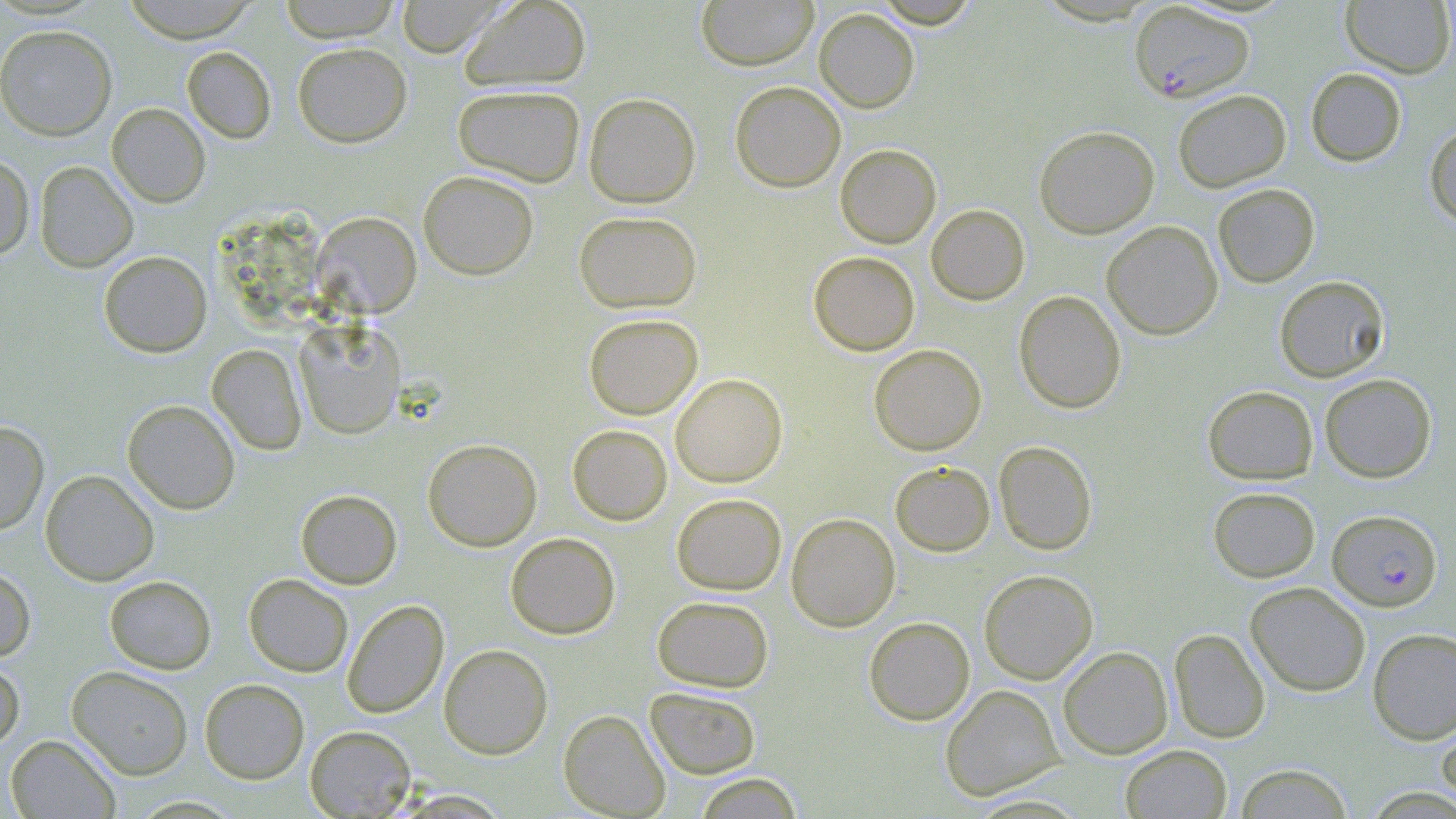

Summary:
  - Coordinate format: approximate bounding boxes as (x1, y1, x2, y2) in pixels
  - Uninfected red blood cell locations: (122, 0, 259, 42), (278, 0, 403, 42), (394, 0, 504, 56), (459, 0, 592, 92), (696, 0, 819, 71), (870, 0, 983, 28), (1340, 0, 1455, 78), (814, 7, 920, 113), (0, 24, 117, 141), (293, 42, 412, 147), (182, 46, 276, 144), (1305, 68, 1407, 166), (730, 81, 846, 193), (452, 84, 586, 186), (1173, 89, 1291, 192), (583, 92, 701, 208), (106, 103, 210, 207), (1425, 123, 1456, 228), (1034, 125, 1159, 238), (835, 143, 941, 248), (0, 153, 35, 260), (34, 160, 139, 272), (418, 170, 539, 279), (1213, 183, 1320, 287), (926, 204, 1030, 305), (573, 210, 702, 313), (312, 212, 422, 317), (1102, 220, 1223, 339), (98, 251, 212, 358), (808, 251, 920, 355), (1274, 275, 1390, 383), (1013, 290, 1127, 413), (583, 313, 703, 419), (294, 320, 406, 439), (207, 344, 306, 455), (869, 344, 986, 456), (670, 373, 788, 487), (1319, 373, 1437, 482), (1202, 385, 1318, 485), (122, 399, 240, 514), (0, 420, 49, 534), (567, 424, 672, 525), (423, 438, 542, 551), (993, 440, 1097, 555), (890, 461, 995, 556), (40, 469, 159, 585), (1208, 486, 1320, 583), (296, 489, 402, 589), (671, 493, 787, 595), (786, 512, 900, 632), (505, 532, 620, 639), (0, 566, 36, 661), (979, 569, 1098, 684), (243, 574, 353, 677), (104, 575, 217, 674), (1245, 581, 1370, 697), (652, 595, 774, 692), (341, 599, 449, 719), (864, 616, 975, 725), (1169, 628, 1270, 743), (1367, 628, 1456, 744), (438, 643, 553, 759), (1058, 646, 1173, 759), (0, 658, 24, 754), (66, 666, 193, 780), (199, 678, 310, 783), (939, 684, 1064, 801), (645, 686, 761, 779), (1435, 709, 1456, 814), (558, 710, 670, 818), (304, 725, 416, 818), (4, 734, 121, 818), (1120, 744, 1232, 818), (1234, 763, 1353, 818), (691, 773, 806, 818)
  - Plasmodium falciparum-infected red blood cell locations: (1127, 2, 1254, 103), (1328, 509, 1442, 611)
  - Slide-level diagnosis: Plasmodium falciparum
  - Magnification: 1000x
  - Stain: May-Grünwald-Giemsa
  - Modality: optical microscopy
  - Field of view: one of a larger specimen
  - Image size: 1456×819 pixels
  - Preparation: thin blood film